Report the malaria status of this cell.
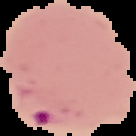
It is parasitized.

image_type: cell region segmented out of the field of view; surrounding area masked to black
image_size: 136×136 pixels
preparation: thin blood film